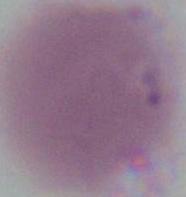

identification = erythrocyte
magnification = 1000x
modality = photomicrograph